Identify the parasite.
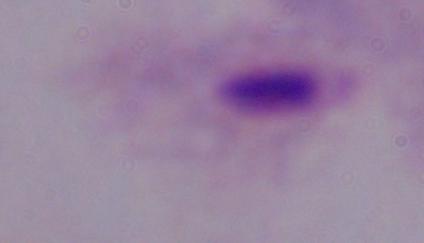
A trichomonad.

{
  "modality": "micrograph",
  "magnification": "1000x"
}